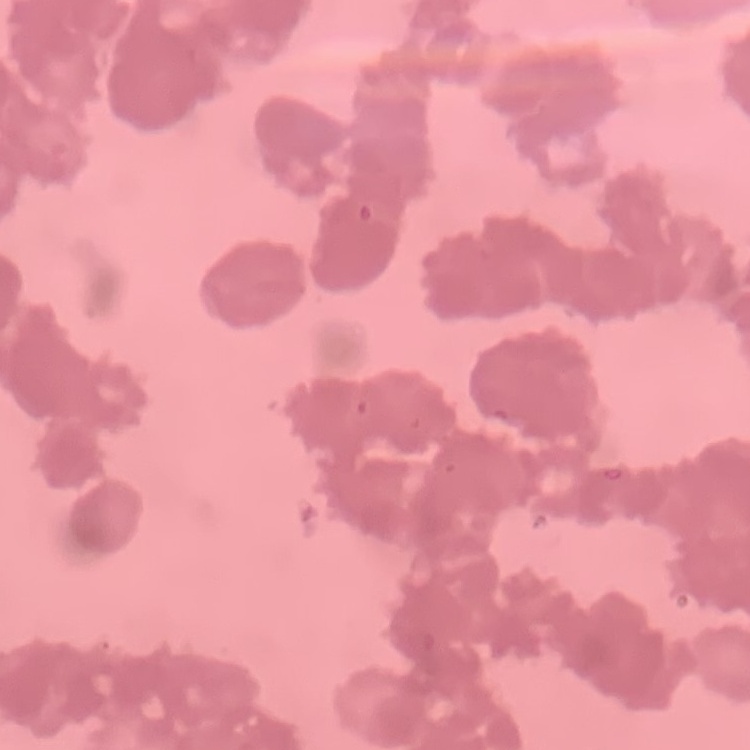

Summary:
  - Red blood cell morphology: rouleaux formation
  - Stain: Field's or Giemsa
  - Preparation: thin blood smear
  - Image type: square crop of a larger photomicrograph